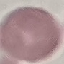
Result: negative for malaria parasites. Cell patch, automatically extracted from a larger field of view and resized to 64 × 64 pixels. Thin smear of blood. Giemsa stain. Photographed with a smartphone camera at the microscope eyepiece.